Draw a bounding box around every leukocyte (white blood cell).
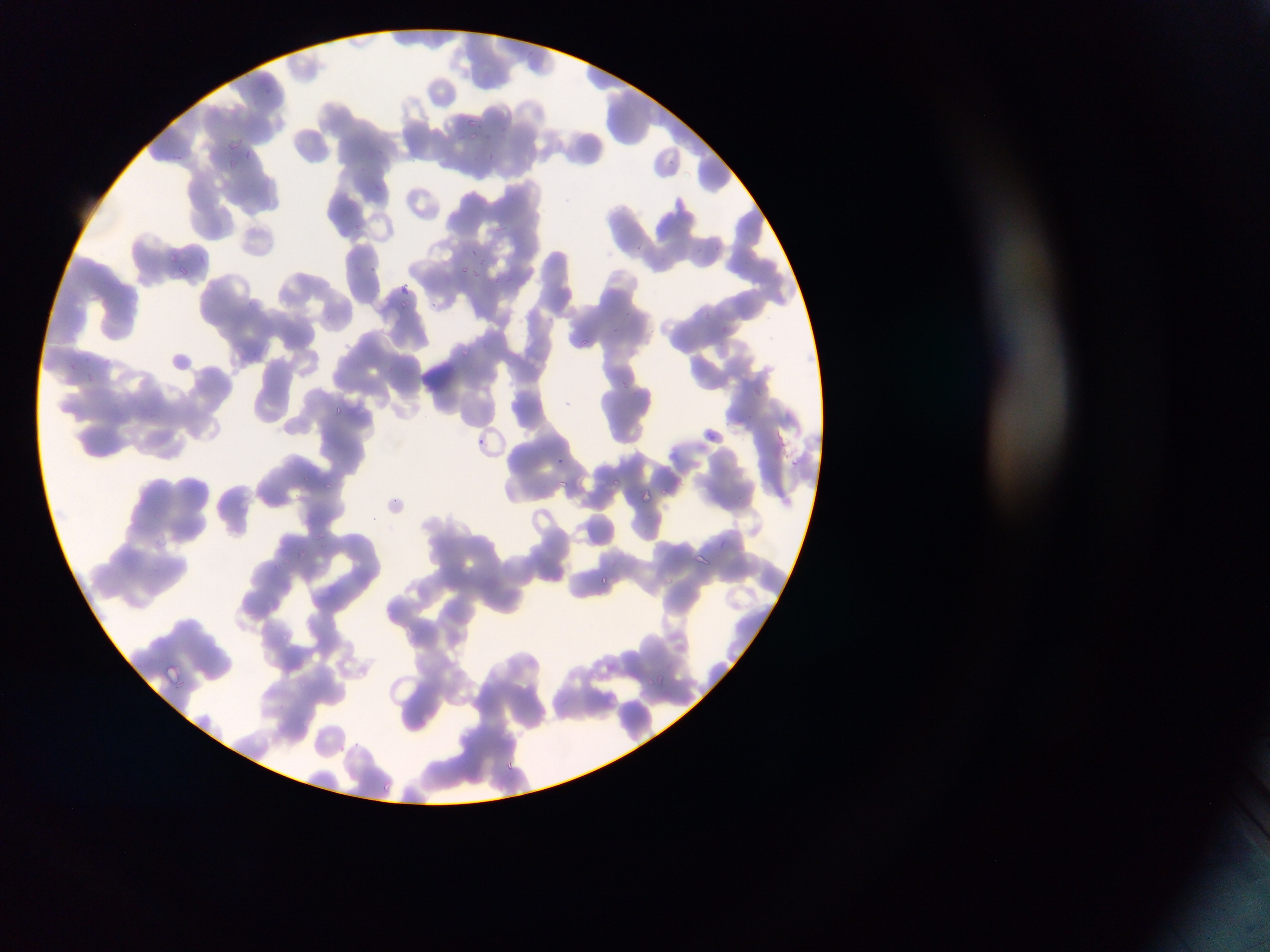

No leukocytes observed.

Approximate bounding boxes as (left, top, right, bottom) in pixels.
Summary:
  - Malaria parasite locations: (466, 112, 479, 127), (463, 122, 489, 142), (224, 134, 245, 149), (481, 151, 498, 167), (228, 158, 254, 185), (699, 244, 718, 262), (468, 245, 482, 258), (166, 250, 183, 267), (457, 263, 475, 278), (169, 264, 192, 284), (398, 295, 415, 308), (698, 310, 713, 324), (570, 333, 593, 353), (457, 345, 473, 360), (617, 375, 634, 392), (331, 402, 349, 419), (704, 429, 720, 443), (612, 477, 630, 495), (325, 480, 332, 490), (556, 480, 568, 493), (641, 485, 657, 500), (148, 530, 179, 556), (318, 533, 332, 540), (299, 550, 308, 559), (692, 552, 714, 572), (594, 571, 616, 591), (157, 663, 185, 689), (652, 669, 671, 688), (509, 758, 529, 778), (379, 780, 395, 796)
  - Preparation: thin blood smear
  - Country: Ghana
  - Image size: 1270×952 pixels
  - Field of view: single
  - Capture: mobile-phone photograph through a microscope